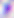
Photomicrograph. Captured at 400x magnification. Toxoplasma gondii is seen.